Assess for malaria.
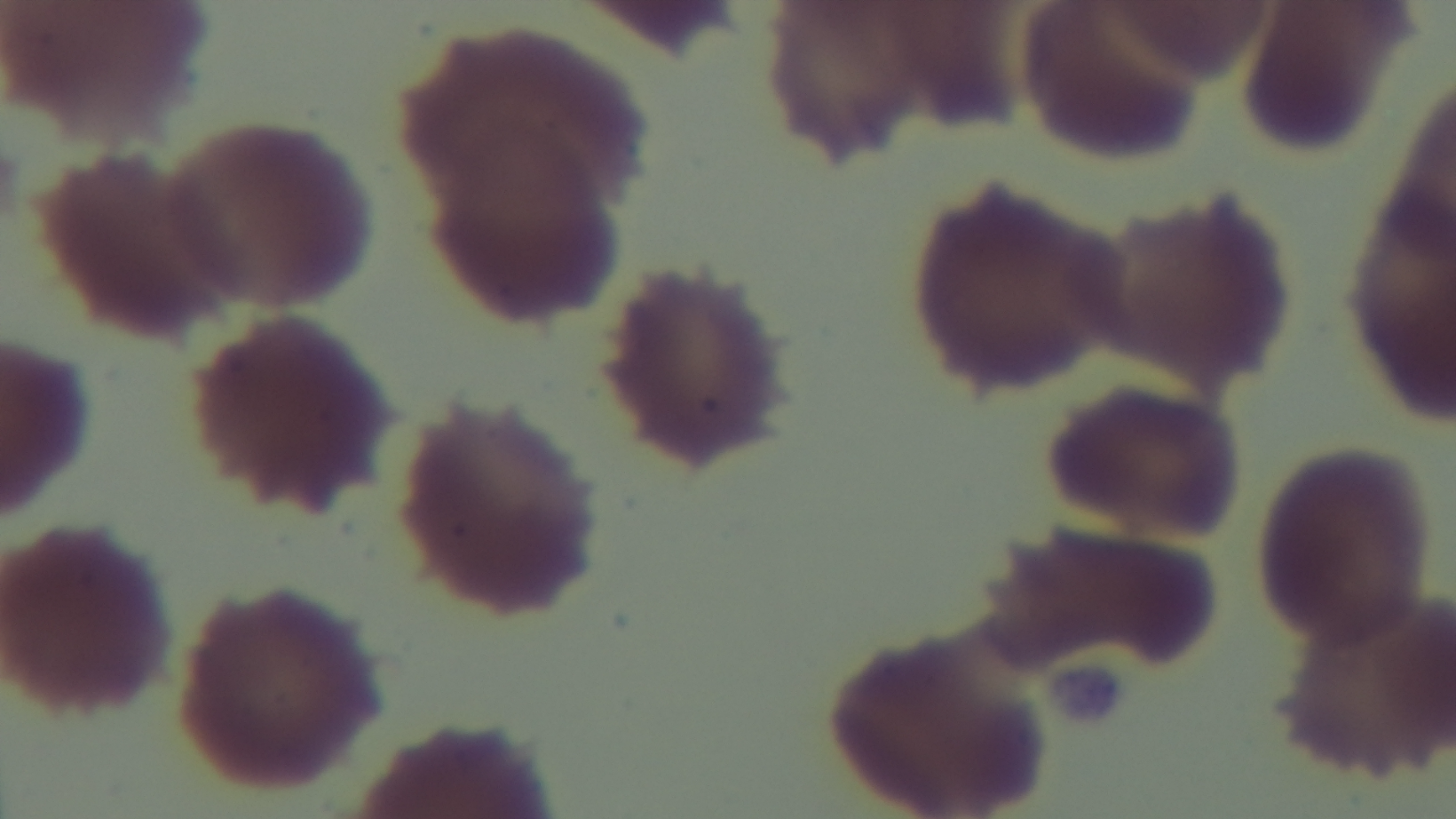
Negative.

Summary:
  - Field of view: one from the slide
  - Objective: 100x oil immersion
  - Stain: Giemsa
  - Capture: mounted 4K digital camera
  - Preparation: thin blood film
  - Modality: light microscopy